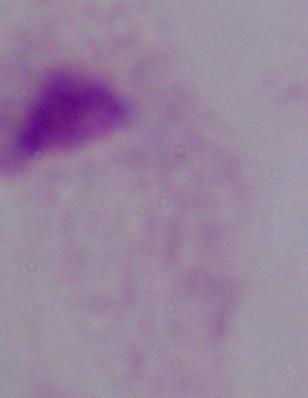

{
  "modality": "photomicrograph",
  "identification": "trichomonad",
  "magnification": "1000x"
}